Assess the morphology of the erythrocytes.
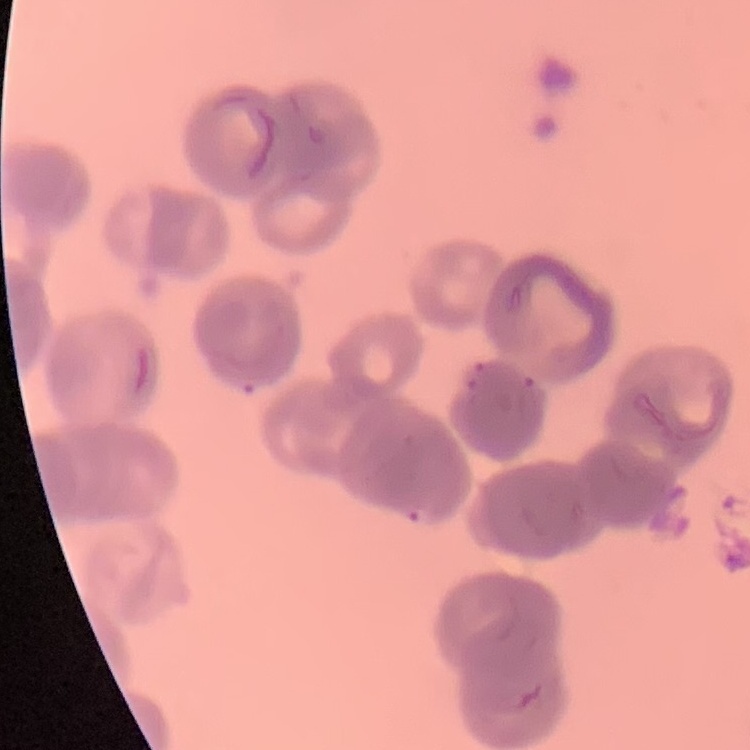
Rouleaux formation.

Field's or Giemsa stain. Thin peripheral smear. One tile cut from a larger photomicrograph.